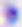
Summary:
  - Magnification: 400x
  - Identification: Toxoplasma gondii
  - Modality: micrograph